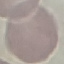
Summary:
  - Malaria status: uninfected
  - Capture: smartphone camera at the microscope eyepiece
  - Preparation: thin smear
  - Image type: cell patch, automatically extracted from a larger field of view and resized to 64 × 64 pixels
  - Stain: Giemsa